State which parasite is depicted.
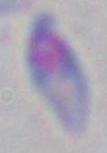

Toxoplasma gondii.

Summary:
  - Modality: micrograph
  - Magnification: 1000x